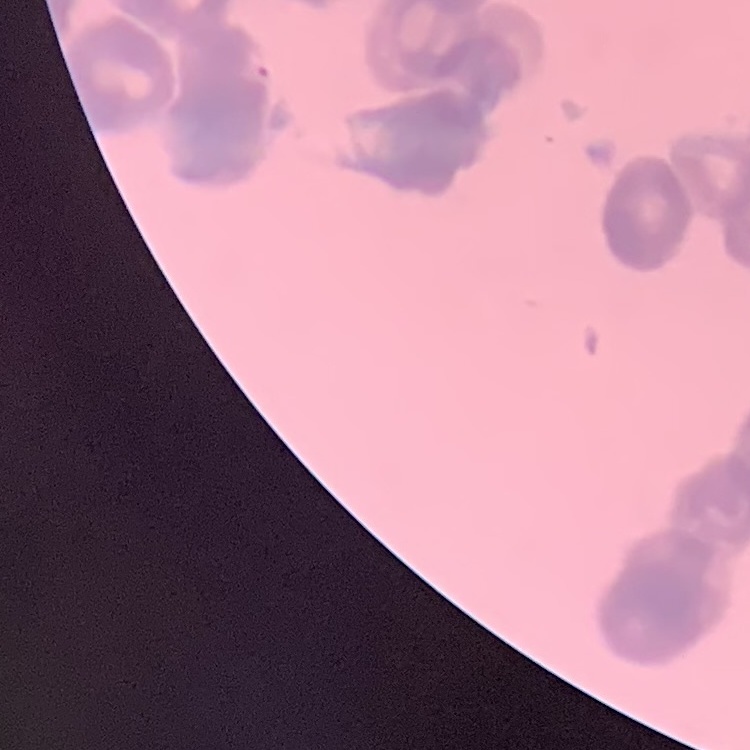

The red blood cells exhibit rouleaux formation. Field's or Giemsa stain. Square crop of a larger photomicrograph. Thin peripheral smear.